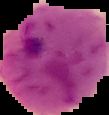
From a thin blood film. Malaria status: parasitized. Image is 109×115 pixels. Segmented cell region on a black background.